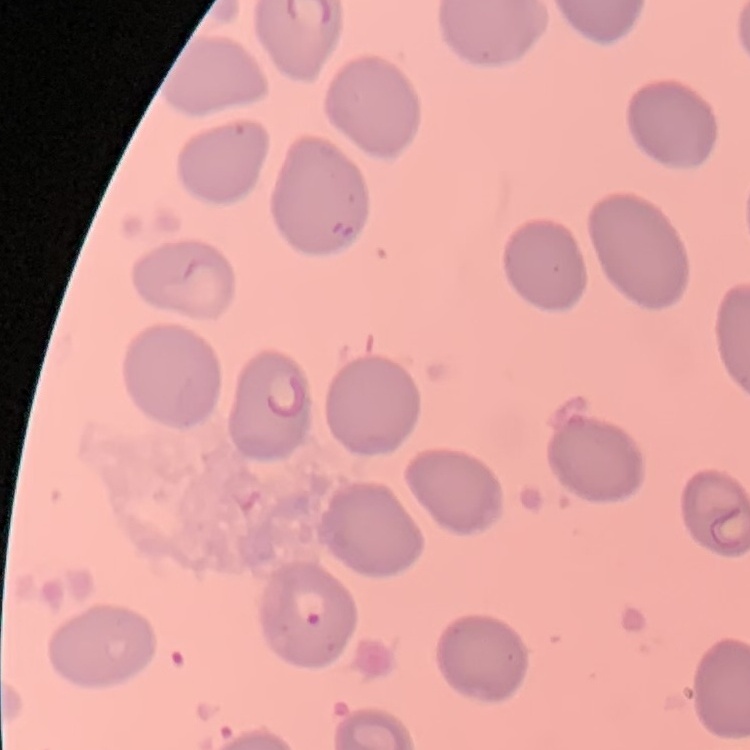
Summary:
  - Erythrocyte morphology: no rouleaux formation
  - Image type: one tile cut from a larger photomicrograph
  - Stain: Field's or Giemsa
  - Preparation: thin peripheral smear